Locate and identify every blood parasite.
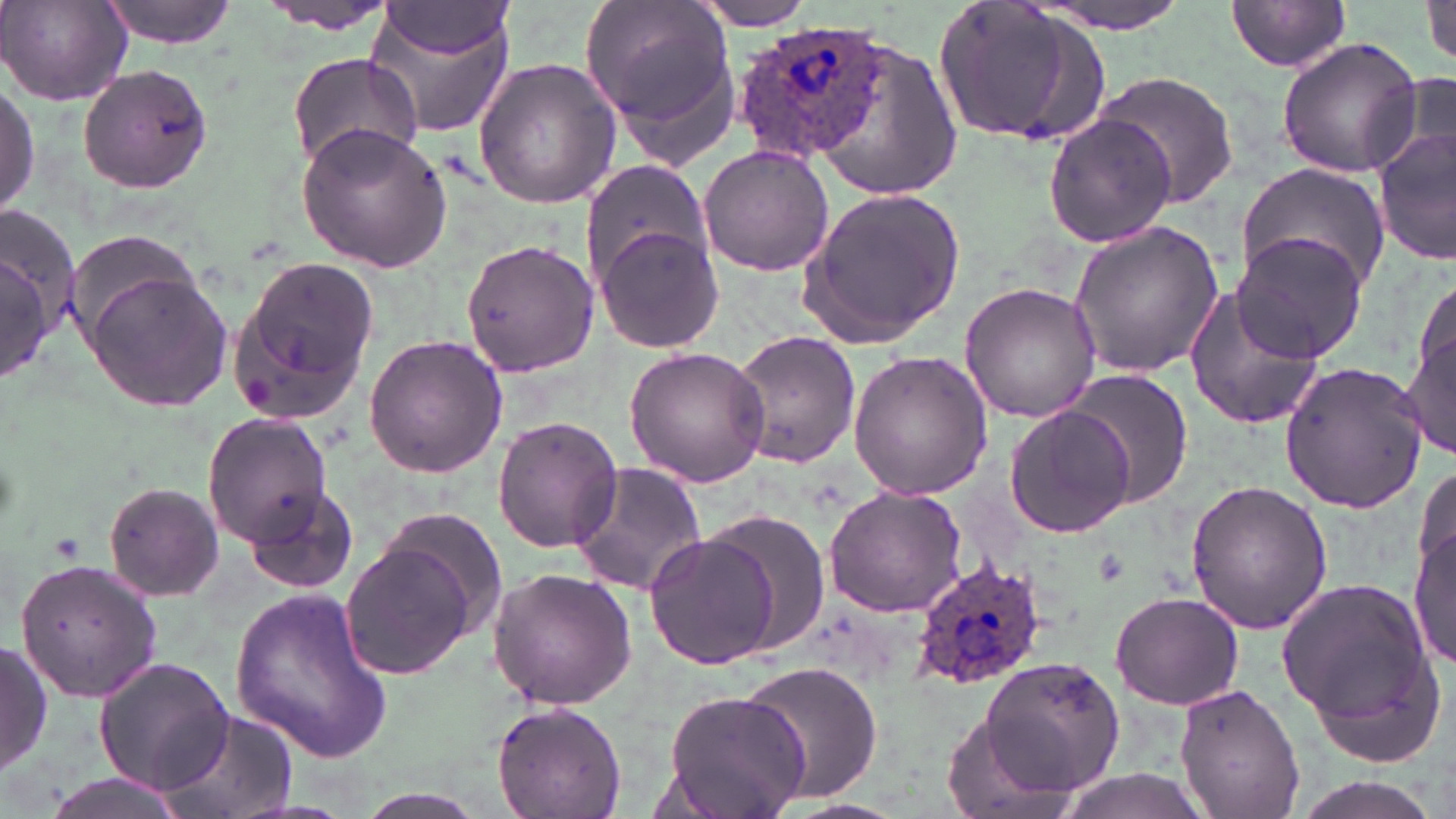
Approximate bounding boxes as (x1, y1, x2, y2) in pixels.
Plasmodium ovale-infected red blood cells: (732, 22, 887, 162), (911, 554, 1048, 690).
No Plasmodium falciparum, Plasmodium malariae, Plasmodium vivax, Babesia divergens, or Trypanosoma brucei observed.

Uninfected red blood cell locations: (98, 0, 237, 47), (257, 0, 405, 34), (582, 0, 740, 160), (1226, 0, 1354, 73), (1424, 0, 1456, 66), (928, 1, 1103, 146), (0, 2, 130, 105), (686, 2, 825, 30), (1026, 2, 1202, 34), (367, 5, 516, 139), (378, 5, 516, 60), (802, 29, 963, 204), (1275, 36, 1425, 179), (286, 54, 422, 169), (473, 57, 622, 208), (77, 62, 215, 194), (1396, 68, 1455, 174), (1093, 70, 1240, 210), (0, 79, 38, 221), (1043, 111, 1179, 250), (295, 123, 451, 271), (1373, 125, 1456, 267), (699, 145, 835, 276), (581, 162, 716, 287), (1236, 164, 1390, 293), (799, 183, 964, 348), (0, 220, 74, 383), (1066, 220, 1225, 379), (595, 225, 726, 352), (62, 228, 207, 344), (1233, 230, 1372, 363), (460, 237, 598, 379), (228, 252, 379, 419), (81, 268, 232, 412), (1182, 280, 1327, 432), (959, 281, 1101, 423), (1402, 311, 1455, 459), (728, 329, 863, 469), (362, 334, 510, 479), (625, 346, 772, 487), (847, 352, 991, 499), (1280, 360, 1428, 513), (1060, 370, 1193, 507), (1003, 402, 1136, 539), (203, 413, 333, 545), (492, 417, 624, 554), (568, 460, 707, 598), (1414, 461, 1455, 609), (1185, 478, 1332, 637), (102, 480, 227, 602), (241, 481, 361, 596), (823, 485, 968, 617), (381, 510, 508, 629), (689, 514, 827, 660), (1412, 517, 1455, 673), (643, 530, 781, 669), (340, 540, 481, 679), (15, 556, 161, 703), (487, 568, 637, 709), (1276, 572, 1445, 762), (229, 585, 392, 765), (1109, 591, 1244, 710), (0, 639, 51, 780), (94, 656, 233, 797), (979, 658, 1125, 797), (736, 659, 884, 810), (1174, 683, 1306, 818), (660, 687, 810, 819), (490, 697, 627, 819), (156, 706, 299, 819), (937, 709, 1076, 819), (1043, 768, 1217, 819), (41, 771, 195, 819). Platelet locations: (1093, 547, 1133, 588). Slide-level diagnosis: Plasmodium ovale. Thin blood film. Light microscopy. May-Grünwald-Giemsa stain. One field of a larger specimen. Image is 1456×819 pixels. Captured at 1000x magnification.